Give the extent of all Plasmodium falciparum-infected red blood cells.
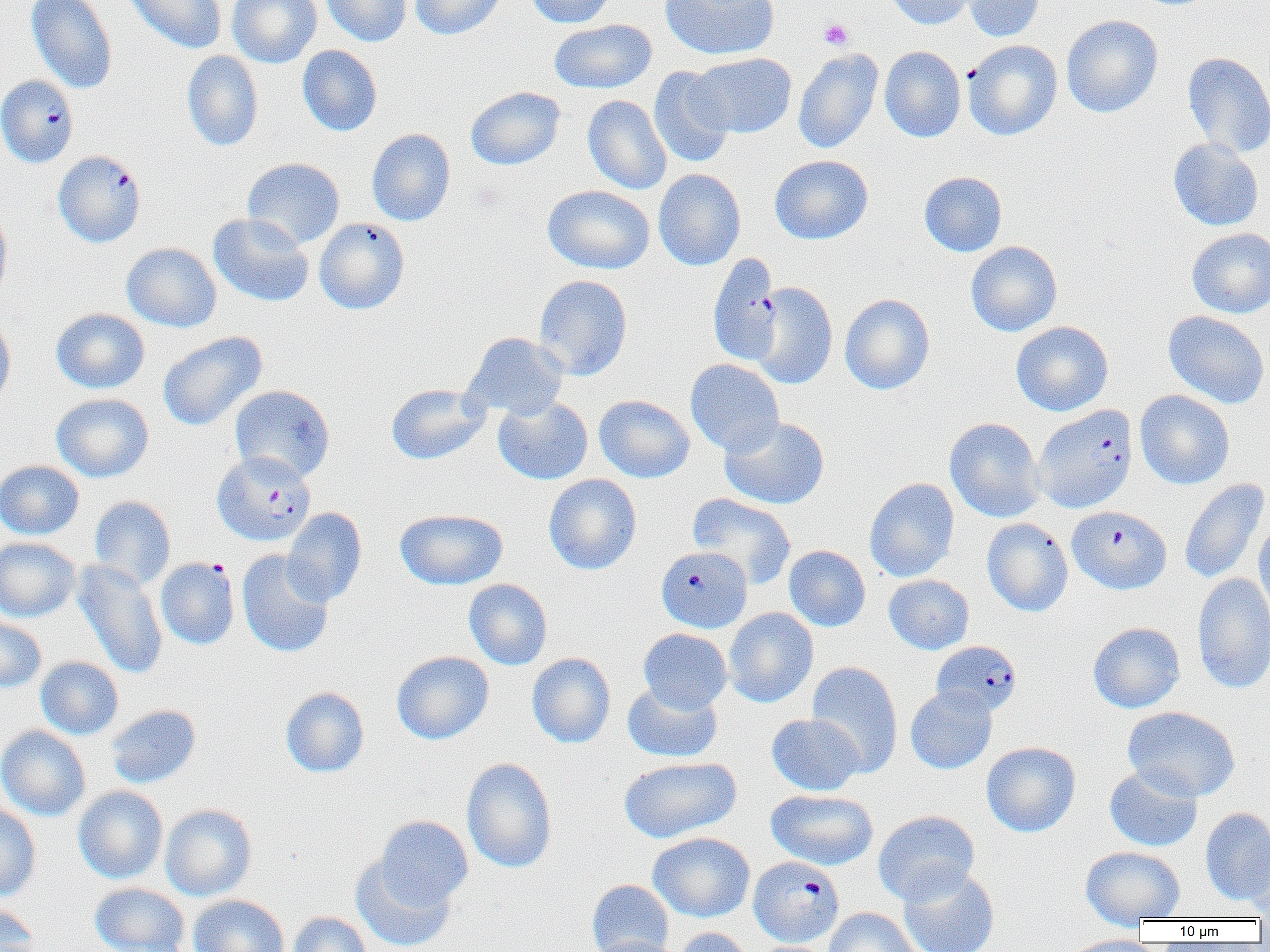

Approximate bounding boxes as (x1, y1, x2, y2) in pixels.
Plasmodium falciparum-infected red blood cells: (0, 75, 79, 167), (53, 150, 147, 247), (707, 253, 782, 366), (1033, 405, 1138, 513), (211, 451, 316, 546), (1067, 505, 1171, 594), (656, 546, 752, 633), (156, 557, 239, 649), (932, 640, 1022, 717), (749, 856, 844, 947).

slide_level_diagnosis: Plasmodium falciparum
magnification: 1000x
preparation: thin blood smear
field_of_view: one of a larger specimen
uninfected_red_blood_cell_locations: 'approximate bounding boxes as (x1, y1, x2, y2) in pixels: (26, 0, 118, 94), (123, 0, 227, 55), (227, 0, 321, 68), (321, 0, 412, 46), (410, 0, 506, 40), (525, 0, 617, 28), (660, 0, 780, 60), (882, 0, 979, 29), (962, 0, 1045, 41), (1061, 14, 1163, 117), (549, 19, 657, 94), (964, 40, 1062, 140), (297, 45, 382, 136), (879, 46, 966, 142), (793, 48, 883, 154), (182, 50, 264, 151), (1182, 52, 1270, 158), (688, 53, 797, 138), (649, 67, 735, 168), (465, 86, 565, 170), (583, 95, 671, 195), (367, 128, 456, 226), (1168, 138, 1264, 231), (769, 155, 873, 245), (243, 157, 345, 248), (653, 169, 746, 270), (919, 171, 1007, 257), (543, 185, 655, 274), (0, 205, 12, 304), (208, 213, 314, 307), (315, 217, 409, 314), (1186, 227, 1270, 318), (966, 241, 1063, 336), (121, 242, 221, 332), (533, 274, 633, 380), (749, 282, 838, 389), (839, 293, 935, 395), (51, 308, 150, 394), (1163, 310, 1270, 409), (0, 313, 16, 410), (1011, 321, 1113, 416), (157, 331, 267, 431), (463, 332, 568, 420), (685, 359, 784, 456), (385, 383, 490, 465), (230, 385, 335, 482), (1135, 389, 1235, 490), (51, 393, 154, 482), (594, 394, 695, 483), (493, 396, 593, 485), (719, 416, 830, 509), (944, 417, 1045, 523), (0, 460, 84, 540), (543, 474, 642, 575), (864, 478, 959, 582), (1179, 478, 1269, 585), (687, 493, 797, 590), (89, 496, 176, 590), (282, 507, 367, 607), (395, 508, 508, 590), (1253, 512, 1270, 625), (982, 518, 1073, 617), (0, 537, 80, 622), (784, 545, 871, 631), (236, 550, 335, 657), (72, 560, 168, 679), (1192, 572, 1270, 694), (884, 574, 974, 654), (464, 579, 552, 670), (723, 607, 818, 708), (0, 617, 46, 693), (1088, 622, 1185, 713), (638, 628, 732, 713), (392, 651, 493, 744), (527, 653, 616, 748), (35, 657, 123, 739), (807, 661, 904, 776), (622, 682, 723, 763), (280, 686, 369, 778), (905, 686, 997, 774), (106, 704, 201, 788), (1123, 706, 1241, 801), (766, 713, 865, 795), (0, 725, 90, 821), (982, 741, 1081, 837), (619, 756, 741, 843), (461, 757, 558, 874), (1105, 764, 1203, 852), (73, 786, 168, 884), (765, 789, 879, 870), (0, 803, 42, 901), (160, 803, 257, 901), (1200, 807, 1270, 905), (873, 810, 980, 905), (375, 815, 472, 910), (1244, 831, 1270, 921), (648, 832, 755, 922), (1081, 846, 1186, 926), (351, 853, 456, 952), (899, 865, 1000, 952), (586, 879, 673, 952), (89, 882, 190, 952), (188, 894, 290, 952), (0, 904, 40, 952), (824, 907, 921, 952), (288, 912, 373, 952), (674, 927, 756, 952), (1060, 934, 1158, 952), (593, 937, 685, 952)'
platelet_locations: 'approximate bounding boxes as (x1, y1, x2, y2) in pixels: (820, 19, 853, 49)'
image_size: 1270×952 pixels
modality: light microscopy